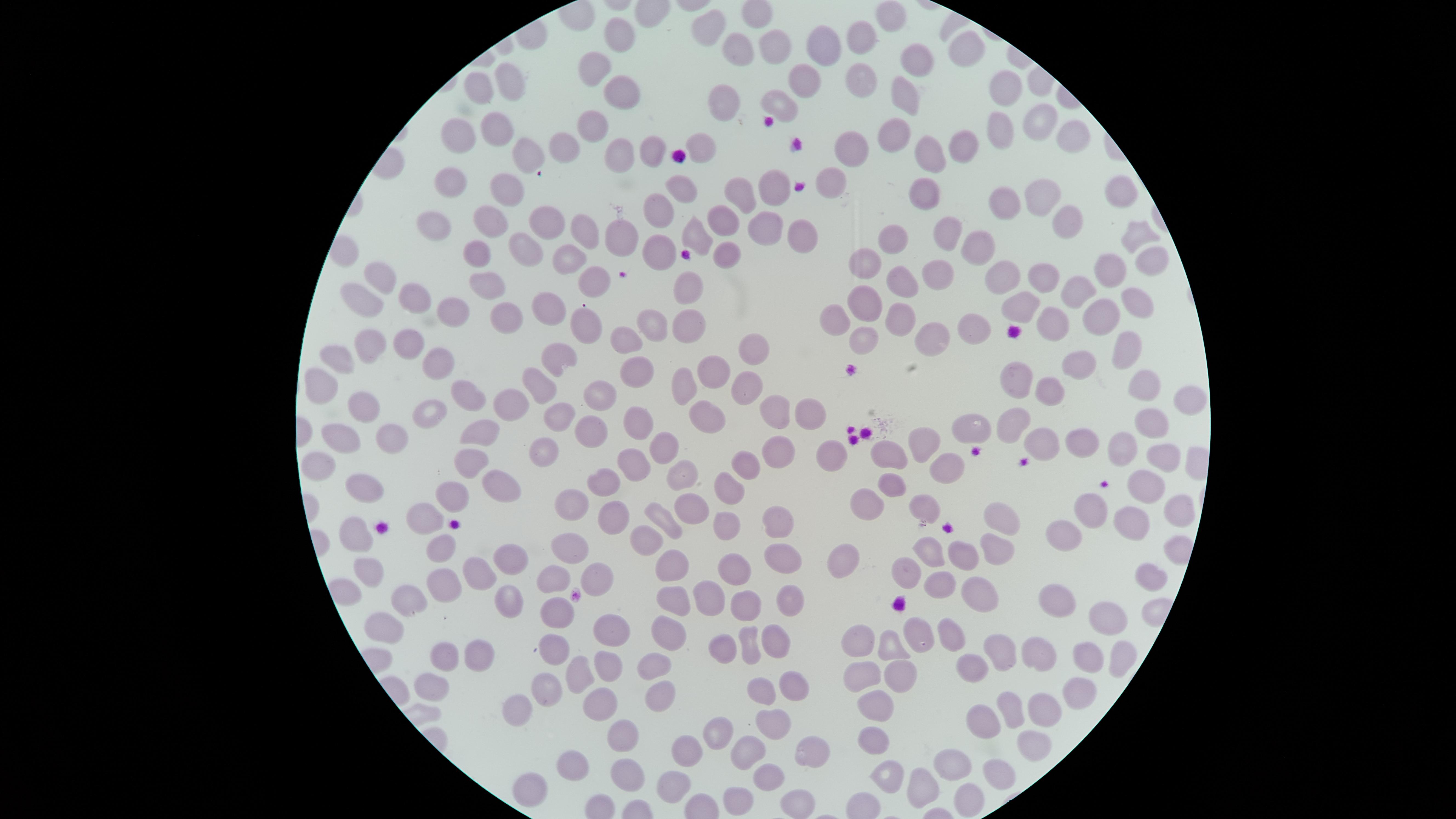 Approximate marker points as {x, y} in pixels. Uninfected RBCs: {887, 13}, {705, 18}, {617, 34}, {863, 36}, {773, 42}, {964, 45}, {822, 48}, {739, 50}, {919, 54}, {594, 68}, {804, 78}, {857, 79}, {509, 83}, {481, 85}, {901, 90}, {1005, 90}, {622, 92}, {781, 103}, {724, 104}, {1043, 119}, {596, 122}, {992, 123}, {498, 125}, {463, 131}, {896, 131}, {1065, 135}, {960, 143}, {701, 144}, {565, 145}, {615, 146}, {849, 149}, {656, 150}, {519, 151}, {931, 153}, {452, 177}, {834, 182}, {769, 183}, {502, 185}, {684, 186}, {739, 190}, {929, 190}, {1041, 190}, {1117, 196}, {1002, 201}, {654, 211}, {725, 220}, {764, 221}, {437, 222}, {547, 222}, {1069, 222}, {493, 223}, {692, 229}, {583, 230}, {622, 231}, {803, 233}, {1140, 233}, {948, 236}, {896, 238}, {982, 248}, {660, 249}, {727, 249}, {527, 250}, {480, 252}, {866, 258}, {567, 259}, {1151, 260}, {1107, 263}, {941, 273}, {1002, 273}, {378, 277}, {596, 278}, {897, 279}, {1043, 279}, {485, 283}, {686, 287}, {361, 292}, {1071, 293}, {861, 297}, {1133, 298}, {414, 299}, {1017, 303}, {548, 306}, {1104, 308}, {450, 310}, {835, 313}, {500, 314}, {901, 316}, {688, 320}, {1051, 320}, {644, 321}, {582, 324}, {975, 326}, {861, 335}, {934, 335}, {620, 340}, {406, 342}, {368, 348}, {751, 349}, {1120, 349}, {338, 357}, {1074, 358}, {551, 359}, {435, 367}, {716, 368}, {631, 374}, {684, 379}, {317, 380}, {743, 380}, {1139, 380}, {1010, 382}, {537, 387}, {1058, 387}, {468, 388}, {599, 392}, {1182, 395}, {506, 402}, {356, 407}, {425, 409}, {778, 410}, {557, 415}, {808, 416}, {705, 417}, {640, 418}, {1015, 421}, {1155, 421}, {587, 426}, {975, 428}, {483, 431}, {392, 436}, {1042, 439}, {341, 440}, {923, 440}, {1079, 441}, {654, 443}, {1127, 445}, {777, 452}, {888, 453}, {540, 454}, {832, 455}, {1161, 456}, {632, 463}, {750, 463}, {468, 464}, {316, 468}, {948, 468}, {674, 470}, {606, 480}, {895, 483}, {501, 484}, {1142, 484}, {364, 485}, {728, 485}, {576, 499}, {447, 500}, {872, 503}, {921, 505}, {689, 506}, {1096, 509}, {426, 513}, {1173, 514}, {619, 518}, {662, 520}, {778, 521}, {723, 523}, {1139, 523}, {1002, 524}, {1062, 530}, {351, 536}, {440, 540}, {643, 542}, {569, 548}, {993, 553}, {930, 554}, {779, 555}, {508, 558}, {961, 558}, {673, 563}, {835, 564}, {367, 565}, {736, 569}, {907, 574}, {556, 575}, {477, 579}, {597, 579}, {1147, 581}, {939, 586}, {442, 590}, {976, 594}, {710, 595}, {408, 597}, {786, 600}, {506, 601}, {668, 602}, {745, 602}, {1056, 602}, {560, 613}, {1103, 618}, {388, 629}, {666, 630}, {613, 633}, {918, 634}, {948, 638}, {774, 641}, {554, 644}, {752, 644}, {860, 646}, {892, 646}, {724, 648}, {995, 651}, {478, 654}, {1037, 654}, {444, 655}, {1082, 658}, {1119, 659}, {605, 660}, {646, 664}, {576, 675}, {858, 675}, {893, 675}, {793, 681}, {433, 683}, {758, 690}, {548, 691}, {656, 691}, {1074, 697}, {875, 699}, {604, 706}, {1040, 706}, {520, 707}, {1011, 708}, {774, 721}, {985, 723}, {722, 730}, {626, 731}, {876, 738}, {1034, 744}, {743, 748}, {694, 750}, {808, 750}, {570, 764}, {951, 768}, {626, 770}, {994, 774}, {767, 776}, {887, 777}, {677, 780}, {922, 782}, {525, 783}, {741, 794}, {965, 799}, {796, 803}. Image is 1456×819 pixels. Thin smear of blood. Giemsa stain. Photographed with a smartphone camera through the microscope eyepiece. The visible region is circular. Presence: no malaria parasites identified. Single field of view.